Locate every uninfected red blood cell.
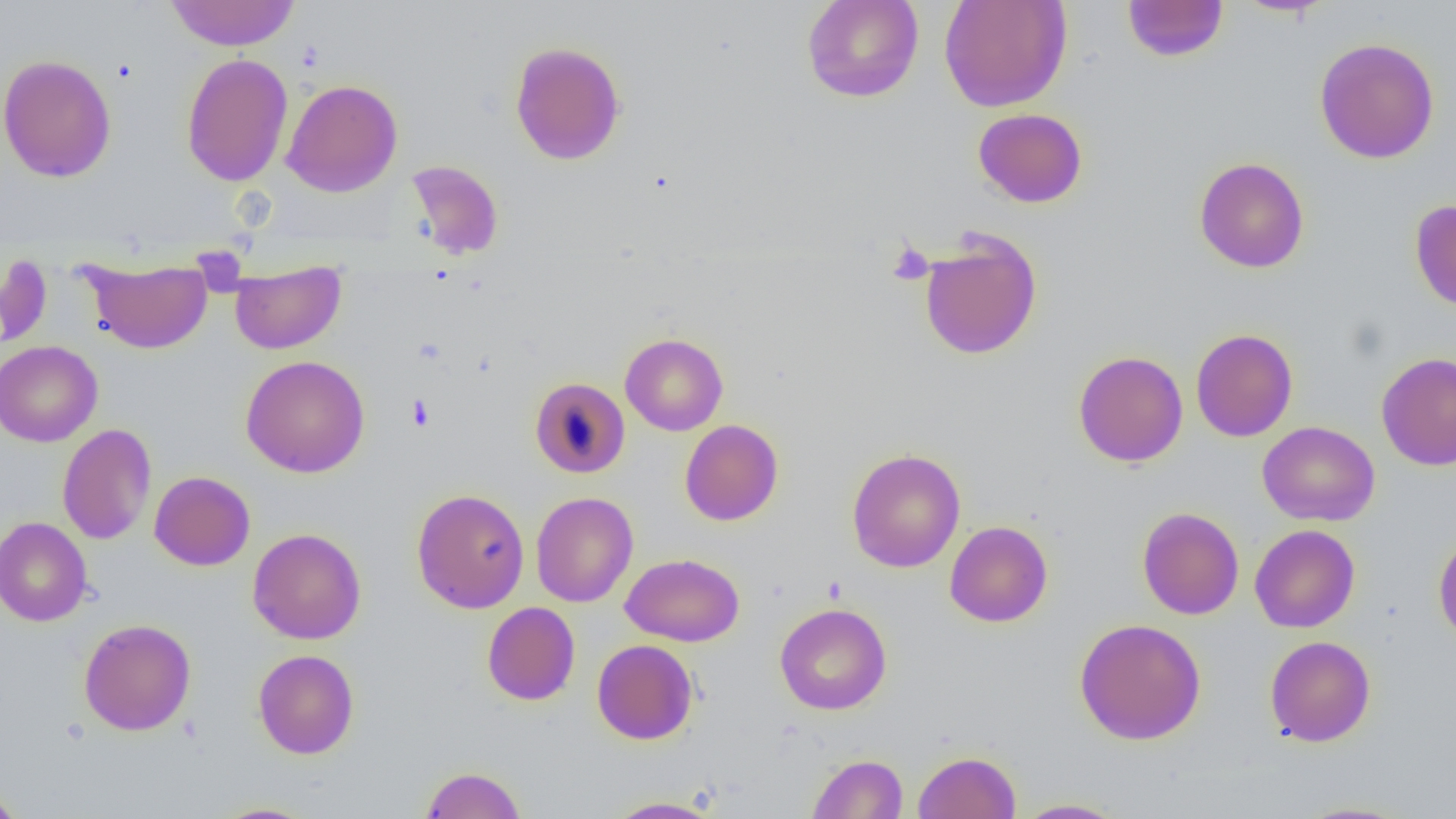
Approximate bounding boxes as (x1,y1)-(x2,y2) corner pairs in pixels.
Uninfected red blood cells: (164,0)-(301,51), (802,0)-(924,103), (939,0)-(1072,112), (1231,0)-(1337,18), (1122,1)-(1229,62), (1314,37)-(1440,164), (509,41)-(626,165), (181,53)-(293,186), (0,54)-(116,182), (281,78)-(403,197), (972,108)-(1088,208), (1194,157)-(1309,273), (404,159)-(504,261), (1410,199)-(1456,312), (919,230)-(1042,361), (0,253)-(52,351), (84,258)-(212,354), (230,263)-(345,354), (1190,328)-(1298,442), (620,332)-(728,436), (0,341)-(103,447), (1072,341)-(1298,449), (1073,351)-(1188,467), (1376,352)-(1456,471), (241,355)-(370,478), (529,376)-(630,478), (679,419)-(783,526), (1258,421)-(1380,526), (58,423)-(157,545), (847,447)-(966,573), (149,471)-(255,571), (411,488)-(529,613), (531,491)-(638,607), (1137,506)-(1244,619), (0,517)-(92,627), (945,521)-(1053,627), (1250,524)-(1360,633), (248,528)-(366,644), (1432,530)-(1456,647), (620,553)-(744,646), (482,601)-(580,705), (774,602)-(892,715), (1074,617)-(1206,745), (78,618)-(196,735), (1264,635)-(1376,747), (592,639)-(698,745), (253,649)-(359,759), (913,750)-(1021,819), (807,753)-(908,818), (420,766)-(526,817), (0,785)-(26,819), (601,796)-(724,818), (1014,798)-(1127,818), (1292,800)-(1417,818), (209,802)-(321,819).

{
  "slide_level_diagnosis": "negative for blood parasites",
  "modality": "light microscopy",
  "image_size": "1456×819 pixels",
  "preparation": "thin blood smear",
  "platelet_locations": "approximate bounding boxes as (x1,y1)-(x2,y2) corner pairs in pixels: (886,241)-(934,286), (407,394)-(433,430)",
  "magnification": "1000x",
  "field_of_view": "one of a larger specimen"
}